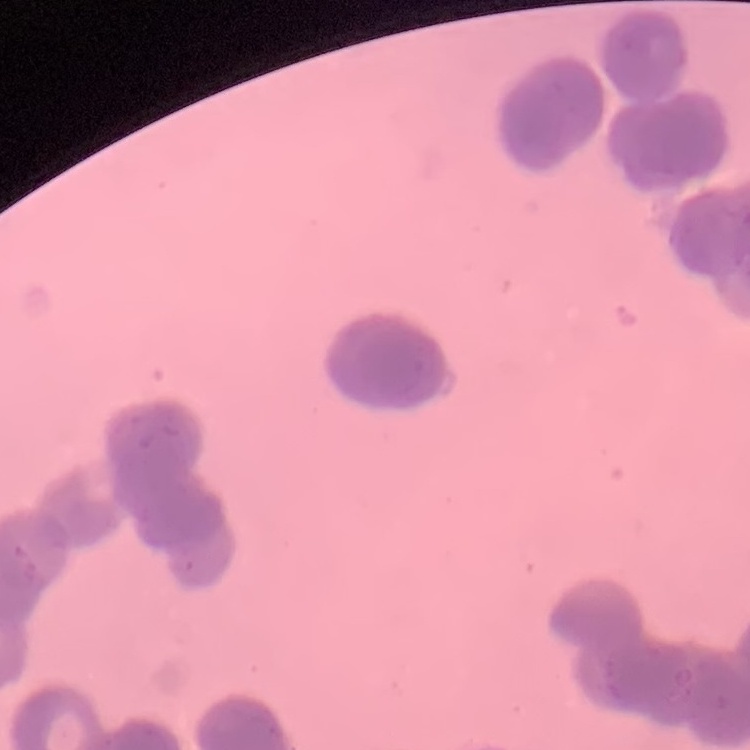
The erythrocytes exhibit rouleaux formation. Field's or Giemsa stain. Thin peripheral smear. Square crop of a larger photomicrograph.